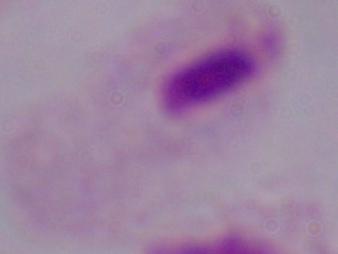 Captured at 1000x magnification. Photomicrograph. A trichomonad is seen.